Identify the parasite.
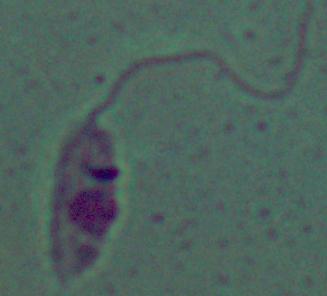

Leishmania.

modality = photomicrograph
magnification = 1000x